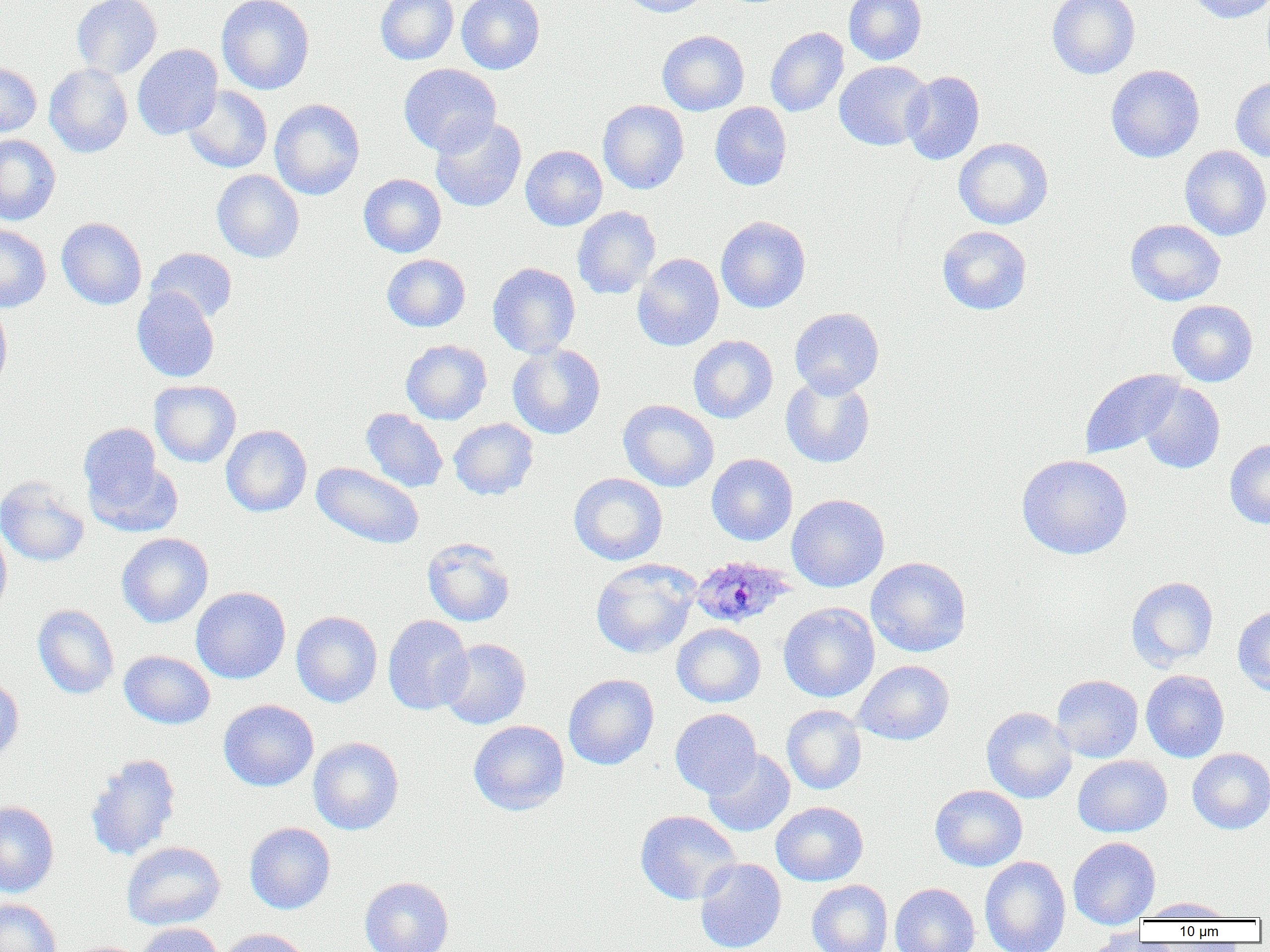
Summary:
  - Coordinate format: approximate bounding boxes as (x1,y1)-(x2,y2) corner pairs in pixels
  - Uninfected red blood cell locations: (71,0)-(162,79), (217,0)-(314,94), (375,0)-(458,65), (456,0)-(545,74), (620,0)-(711,17), (844,0)-(927,65), (1046,0)-(1140,79), (1185,0)-(1270,23), (765,26)-(849,117), (657,30)-(749,115), (132,44)-(222,140), (834,60)-(933,150), (0,61)-(41,138), (45,64)-(133,157), (398,64)-(500,156), (1106,65)-(1205,162), (902,70)-(985,165), (1231,77)-(1270,162), (182,86)-(272,173), (269,98)-(365,200), (598,100)-(689,194), (710,102)-(792,190), (430,115)-(527,212), (0,135)-(61,225), (953,137)-(1054,229), (520,145)-(607,231), (1180,146)-(1270,241), (212,170)-(304,263), (358,174)-(447,257), (572,206)-(661,299), (715,216)-(811,313), (56,217)-(147,310), (1125,219)-(1225,306), (0,224)-(51,313), (937,225)-(1032,315), (145,248)-(237,324), (633,253)-(724,351), (382,254)-(470,331), (487,262)-(580,358), (132,288)-(220,383), (0,300)-(12,398), (1167,300)-(1258,386), (789,307)-(884,398), (688,335)-(778,423), (401,340)-(492,424), (507,344)-(606,439), (1080,369)-(1184,459), (781,376)-(875,468), (149,380)-(241,467), (1138,381)-(1225,474), (618,399)-(719,492), (361,408)-(448,493), (449,418)-(539,500), (79,423)-(163,511), (221,425)-(312,517), (1225,438)-(1270,529), (83,452)-(182,539), (706,453)-(798,546), (1017,454)-(1132,559), (311,462)-(424,550), (568,472)-(668,565), (0,477)-(89,567), (787,494)-(889,592), (0,523)-(12,619), (117,533)-(214,628), (422,537)-(516,627), (865,556)-(971,657), (590,558)-(700,658), (1126,577)-(1219,670), (191,586)-(291,684), (778,602)-(879,702), (33,605)-(119,699), (1232,606)-(1270,696), (291,611)-(383,707), (383,615)-(473,715), (671,623)-(766,708), (439,638)-(531,729), (118,651)-(215,729), (853,660)-(954,745), (1140,669)-(1229,762), (563,674)-(659,770), (1051,674)-(1143,762), (0,676)-(24,765), (218,699)-(318,791), (782,705)-(867,794), (981,707)-(1077,803), (670,708)-(762,797), (468,720)-(569,815), (308,737)-(404,835), (1187,748)-(1270,834), (703,749)-(796,837), (85,753)-(182,861), (1073,755)-(1172,837), (929,784)-(1028,871), (0,801)-(59,897), (770,801)-(868,886), (635,810)-(740,905), (244,822)-(336,914), (1068,836)-(1160,929), (121,841)-(225,930), (980,856)-(1071,952), (694,858)-(787,952), (359,876)-(453,952), (806,879)-(893,952), (890,883)-(980,952), (0,897)-(61,952), (1138,897)-(1236,921), (135,922)-(224,952), (1079,926)-(1156,952), (217,928)-(312,952)
  - Plasmodium ovale-infected red blood cell locations: (691,555)-(794,629)
  - Slide-level diagnosis: Plasmodium ovale
  - Image size: 1270×952 pixels
  - Preparation: thin blood smear
  - Magnification: 1000x
  - Modality: light microscopy
  - Field of view: single